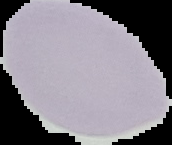

Image is 172×145 pixels. The area outside the segmented cell region is set to black. From a thin blood smear. Malaria status: uninfected.